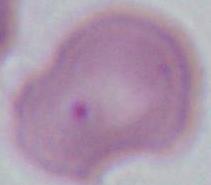

Summary:
  - Magnification: 1000x
  - Modality: photomicrograph
  - Identification: erythrocyte